Give the position of every leukocyte visible.
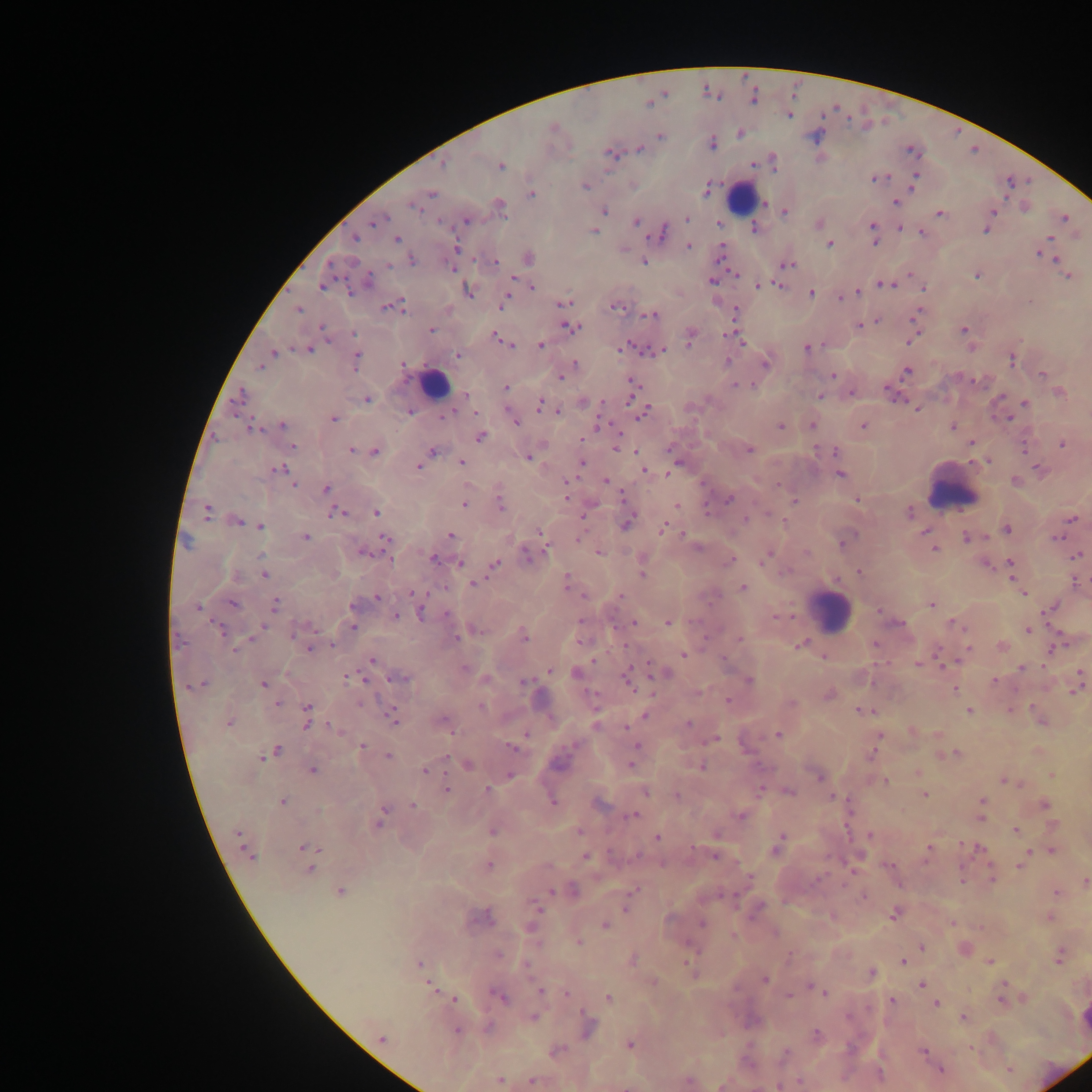

Approximate centers as {x, y} in pixels.
Leukocytes: {742, 196}, {435, 383}, {952, 486}, {830, 609}.

{
  "plasmodium_parasite_locations": "approximate centers as {x, y} in pixels: {753, 97}, {789, 114}, {554, 127}, {740, 134}, {660, 136}, {815, 137}, {712, 143}, {639, 150}, {911, 150}, {611, 153}, {443, 164}, {501, 166}, {877, 178}, {914, 182}, {585, 185}, {707, 190}, {432, 193}, {531, 193}, {896, 203}, {414, 207}, {501, 207}, {604, 211}, {784, 212}, {993, 212}, {941, 213}, {1065, 217}, {687, 218}, {376, 220}, {467, 220}, {441, 221}, {636, 221}, {718, 224}, {818, 224}, {754, 228}, {873, 228}, {900, 228}, {594, 231}, {986, 231}, {921, 232}, {662, 233}, {1050, 238}, {355, 239}, {396, 239}, {829, 245}, {688, 246}, {456, 249}, {1040, 253}, {529, 258}, {1053, 258}, {412, 260}, {495, 261}, {645, 263}, {388, 265}, {787, 265}, {976, 275}, {1068, 275}, {368, 281}, {712, 281}, {885, 285}, {321, 286}, {759, 286}, {923, 287}, {533, 288}, {468, 292}, {857, 292}, {810, 293}, {842, 297}, {1029, 301}, {504, 302}, {564, 303}, {398, 305}, {385, 307}, {616, 307}, {299, 309}, {735, 310}, {653, 315}, {860, 325}, {322, 327}, {570, 327}, {431, 329}, {964, 329}, {354, 333}, {690, 337}, {496, 338}, {739, 339}, {910, 341}, {502, 342}, {508, 344}, {540, 345}, {623, 348}, {309, 349}, {807, 349}, {656, 351}, {274, 352}, {457, 355}, {1012, 359}, {356, 360}, {728, 361}, {574, 363}, {766, 363}, {402, 365}, {259, 367}, {906, 371}, {1042, 374}, {832, 375}, {561, 376}, {633, 383}, {737, 386}, {506, 388}, {851, 393}, {1060, 393}, {240, 395}, {466, 395}, {821, 396}, {367, 400}, {1025, 403}, {540, 405}, {917, 409}, {410, 411}, {559, 412}, {642, 412}, {448, 414}, {333, 418}, {1004, 418}, {515, 422}, {283, 425}, {812, 425}, {863, 425}, {253, 427}, {781, 427}, {953, 427}, {480, 437}, {970, 443}, {1062, 444}, {293, 446}, {619, 449}, {351, 450}, {749, 450}, {375, 451}, {432, 451}, {835, 451}, {528, 458}, {462, 463}, {581, 463}, {677, 465}, {418, 466}, {279, 469}, {644, 470}, {1039, 470}, {840, 474}, {606, 480}, {1015, 480}, {293, 485}, {326, 489}, {566, 496}, {729, 499}, {857, 500}, {795, 501}, {500, 503}, {464, 505}, {676, 505}, {376, 512}, {206, 513}, {336, 513}, {908, 513}, {745, 519}, {1072, 519}, {238, 522}, {627, 523}, {261, 526}, {663, 528}, {1007, 529}, {540, 531}, {925, 532}, {450, 535}, {305, 537}, {1056, 537}, {385, 538}, {579, 538}, {966, 538}, {845, 541}, {698, 547}, {933, 549}, {362, 553}, {599, 553}, {806, 553}, {527, 555}, {766, 556}, {1078, 556}, {433, 558}, {390, 560}, {730, 560}, {459, 563}, {495, 564}, {1010, 564}, {987, 565}, {859, 571}, {642, 574}, {265, 575}, {236, 577}, {567, 581}, {1075, 583}, {473, 584}, {743, 587}, {1017, 588}, {414, 593}, {1023, 593}, {620, 595}, {377, 598}, {233, 604}, {276, 605}, {931, 605}, {353, 606}, {197, 607}, {1052, 607}, {879, 611}, {421, 613}, {396, 616}, {580, 622}, {632, 622}, {669, 622}, {899, 623}, {956, 624}, {264, 626}, {352, 628}, {219, 629}, {1029, 630}, {294, 634}, {456, 637}, {524, 637}, {252, 639}, {739, 639}, {332, 645}, {800, 645}, {875, 645}, {1002, 647}, {1056, 648}, {308, 649}, {968, 649}, {235, 650}, {683, 655}, {823, 658}, {372, 660}, {920, 663}, {466, 668}, {1021, 668}, {549, 670}, {663, 671}, {577, 673}, {350, 677}, {400, 678}, {626, 679}, {750, 680}, {994, 681}, {1079, 681}, {523, 682}, {204, 684}, {263, 684}, {955, 689}, {1077, 689}, {828, 695}, {728, 701}, {360, 703}, {277, 704}, {792, 704}, {307, 707}, {482, 707}, {860, 710}, {969, 711}, {645, 716}, {393, 719}, {443, 722}, {229, 723}, {688, 723}, {596, 725}, {306, 726}, {333, 728}, {626, 728}, {911, 731}, {526, 735}, {777, 735}, {713, 738}, {878, 739}, {636, 745}, {362, 746}, {511, 748}, {277, 751}, {956, 753}, {271, 754}, {871, 754}, {388, 756}, {262, 758}, {468, 765}, {631, 765}, {700, 767}, {313, 770}, {425, 770}, {918, 771}, {510, 774}, {1052, 776}, {819, 777}, {1005, 780}, {886, 782}, {1009, 782}, {761, 789}, {487, 790}, {446, 791}, {645, 792}, {790, 792}, {925, 795}, {677, 796}, {833, 798}, {283, 801}, {553, 802}, {982, 802}, {599, 803}, {412, 805}, {1044, 805}, {981, 808}, {319, 810}, {384, 811}, {633, 816}, {740, 816}, {980, 817}, {379, 823}, {1015, 830}, {492, 832}, {579, 832}, {238, 833}, {716, 834}, {870, 835}, {657, 838}, {780, 840}, {306, 847}, {776, 849}, {980, 849}, {929, 850}, {1052, 852}, {1026, 853}, {249, 855}, {586, 856}, {715, 857}, {1021, 865}, {489, 866}, {888, 866}, {311, 868}, {962, 878}, {818, 879}, {992, 879}, {1085, 880}, {633, 890}, {551, 891}, {574, 891}, {341, 892}, {1057, 892}, {537, 907}, {626, 908}, {894, 915}, {1049, 917}, {483, 919}, {702, 922}, {952, 922}, {605, 926}, {733, 935}, {579, 943}, {921, 947}, {498, 955}, {790, 956}, {1059, 959}, {633, 960}, {902, 961}, {686, 962}, {989, 962}, {419, 964}, {871, 973}, {765, 980}, {653, 982}, {922, 984}, {430, 986}, {540, 990}, {817, 990}, {823, 992}, {566, 993}, {788, 996}, {500, 997}, {608, 997}, {454, 999}, {891, 1001}, {1001, 1001}, {936, 1004}, {848, 1016}, {533, 1018}, {964, 1018}, {489, 1027}, {588, 1029}, {457, 1031}, {817, 1034}, {382, 1038}, {630, 1045}, {556, 1051}, {922, 1051}, {786, 1052}, {941, 1070}, {500, 1080}, {688, 1080}, {532, 1081}, {799, 1081}",
  "preparation": "thick blood smear",
  "country": "Ghana",
  "image_size": "1092×1092 pixels",
  "capture": "mobile-phone photograph through a microscope",
  "field_of_view": "single"
}